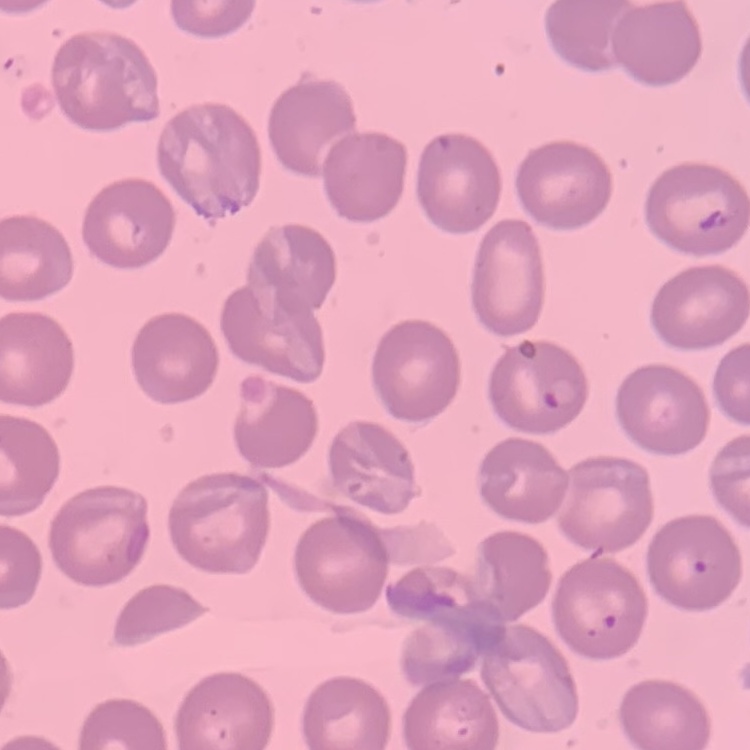

Summary:
  - Red blood cell morphology: no rouleaux formation
  - Image type: square crop of a larger photomicrograph
  - Preparation: thin peripheral smear
  - Stain: Field's or Giemsa